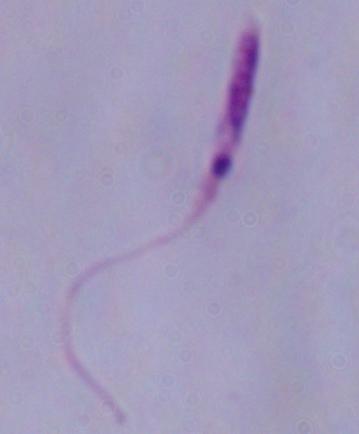
Summary:
  - Magnification: 1000x
  - Identification: Leishmania
  - Modality: photomicrograph